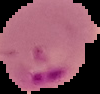
{
  "preparation": "thin blood smear",
  "image_type": "segmented cell region on a black background",
  "result": "Plasmodium parasites identified",
  "image_size": "100×94 pixels"
}